Assess the morphology of the erythrocytes.
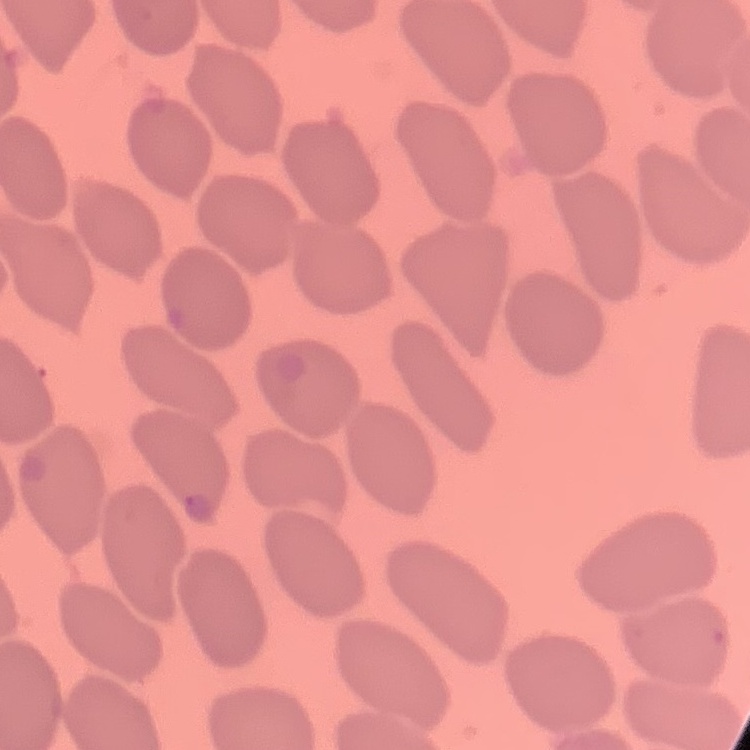

No rouleaux formation.

{
  "preparation": "thin blood film",
  "image_type": "one tile cut from a larger photomicrograph",
  "stain": "Field's or Giemsa"
}